Describe the morphology of the erythrocytes.
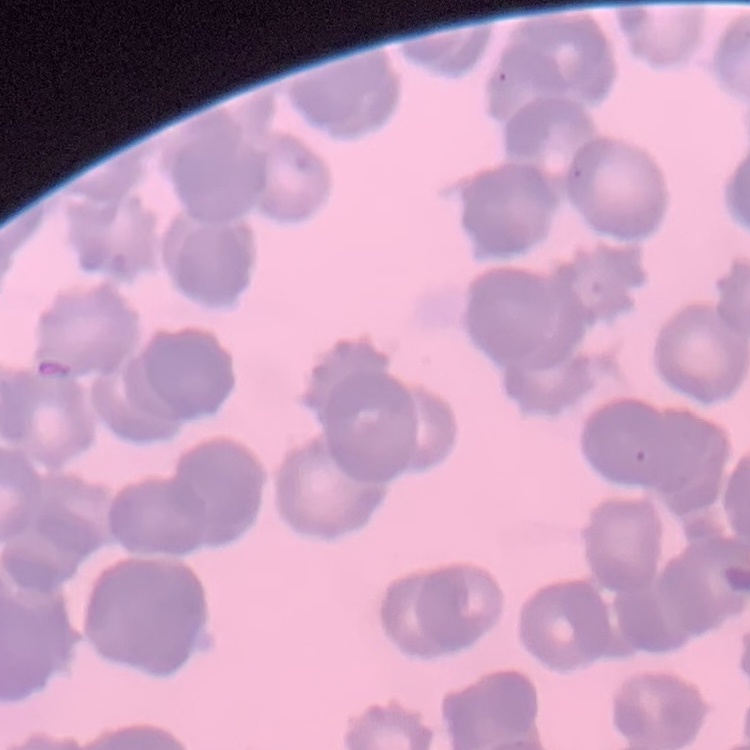
Rouleaux formation.

Field's or Giemsa stain. One tile cut from a larger photomicrograph. Thin peripheral smear.